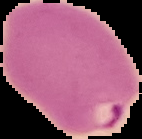

Summary:
  - Result: malaria parasites detected
  - Preparation: thin blood smear
  - Image size: 142×139 pixels
  - Image type: cell region segmented out of the field of view; surrounding area masked to black